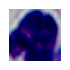

Summary:
  - Magnification: 1000x
  - Identification: white blood cell
  - Modality: micrograph